Assess this cell for malaria.
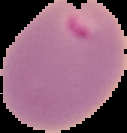
Parasitized.

Summary:
  - Image size: 127×133 pixels
  - Preparation: thin blood smear
  - Image type: cell region segmented out of the field of view; surrounding area masked to black